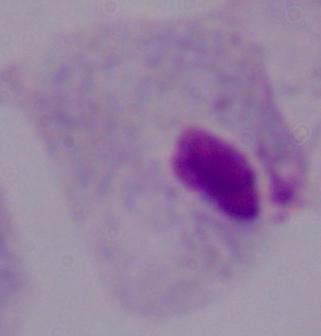

magnification = 1000x
modality = micrograph
identification = trichomonad